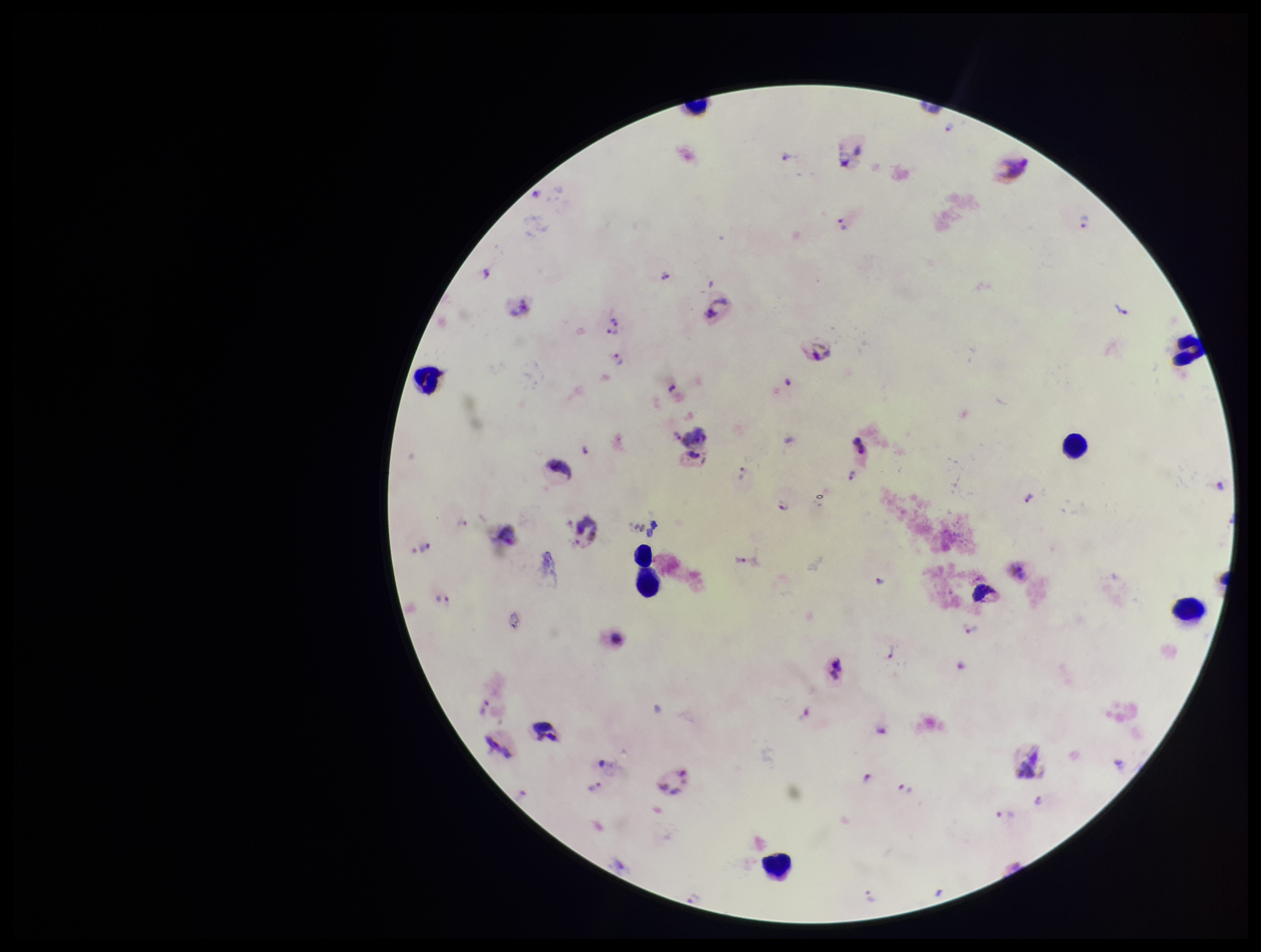

{
  "stain": "Giemsa",
  "preparation": "thick",
  "plasmodium_parasites": "identified",
  "species_reported_for_this_patient": "Plasmodium vivax",
  "parasite_count": 21,
  "patient_malaria_status": "positive",
  "field_of_view": "single",
  "image_size": "1261×952 pixels",
  "capture": "smartphone photograph through the microscope eyepiece",
  "leukocyte_count": 8
}